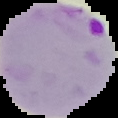

Summary:
  - Image size: 118×118 pixels
  - Preparation: thin blood film
  - Malaria status: parasitized
  - Image type: segmented cell region on a black background